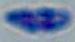
Micrograph. Toxoplasma gondii is seen. Captured at 1000x magnification.